Locate and identify every blood parasite.
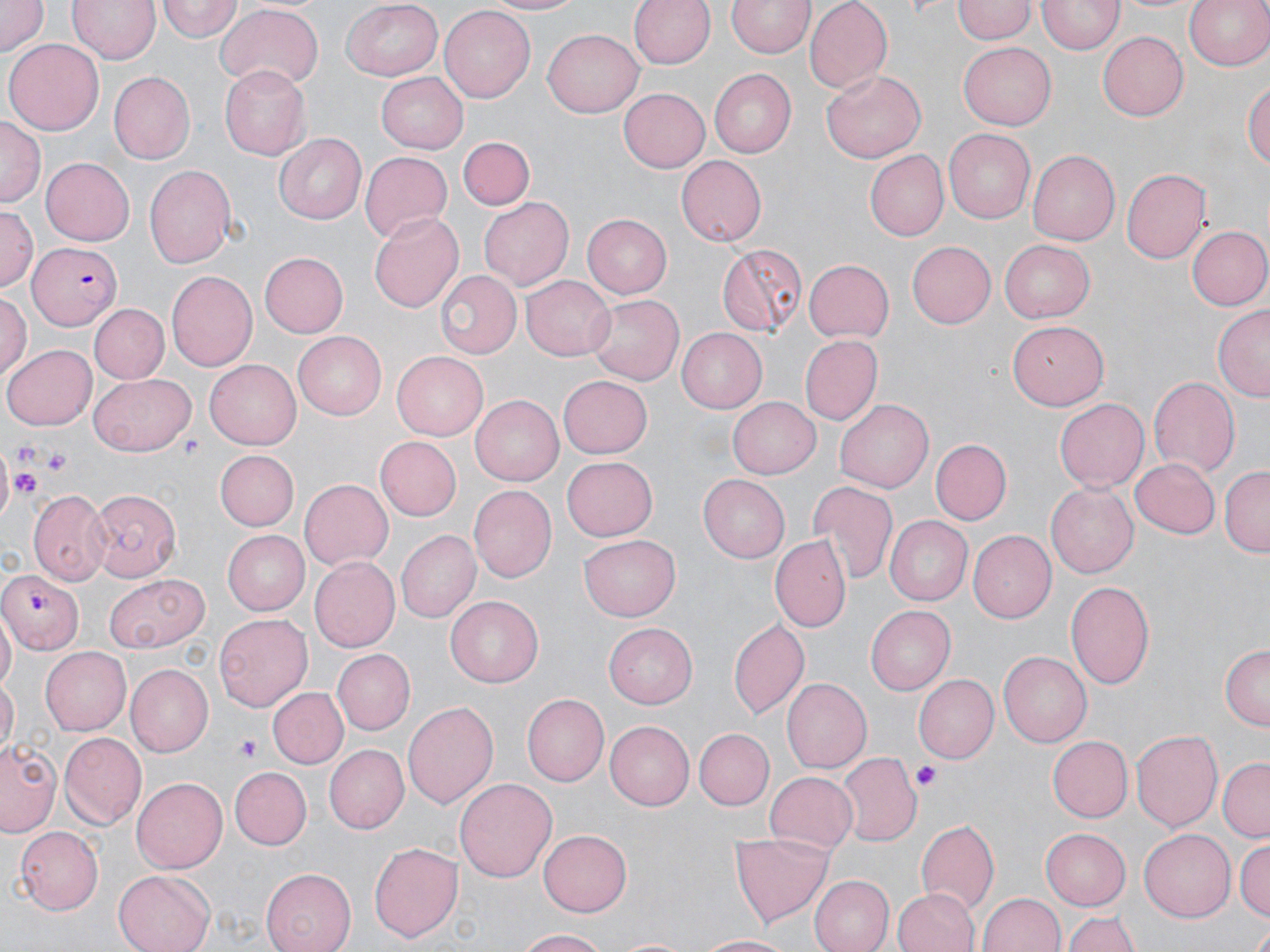
Approximate bounding boxes as (x1, y1, x2, y2) in pixels.
Plasmodium falciparum-infected red blood cells: (30, 240, 120, 331), (0, 569, 84, 653).
No Plasmodium ovale, Plasmodium malariae, Plasmodium vivax, Babesia divergens, or Trypanosoma brucei observed.

Platelet locations: (13, 444, 38, 470), (46, 450, 71, 476), (8, 468, 43, 500), (236, 735, 265, 759), (910, 762, 942, 791). Uninfected red blood cell locations: (0, 0, 48, 57), (68, 0, 160, 65), (478, 0, 589, 17), (630, 0, 715, 70), (804, 0, 892, 91), (1115, 0, 1211, 17), (1184, 0, 1270, 72), (158, 1, 241, 44), (340, 1, 444, 80), (727, 1, 813, 59), (953, 2, 1036, 44), (1038, 2, 1121, 55), (214, 5, 326, 88), (439, 6, 533, 104), (543, 28, 643, 116), (1098, 30, 1187, 119), (5, 39, 104, 136), (960, 41, 1055, 129), (218, 64, 310, 159), (709, 69, 796, 158), (822, 69, 926, 164), (108, 71, 195, 165), (375, 72, 468, 152), (1245, 76, 1270, 177), (618, 86, 712, 172), (0, 119, 44, 205), (943, 129, 1035, 224), (273, 133, 366, 224), (458, 134, 535, 210), (1028, 150, 1119, 244), (360, 151, 452, 242), (866, 152, 948, 240), (675, 155, 766, 247), (40, 156, 135, 246), (144, 166, 239, 270), (1121, 168, 1210, 266), (477, 195, 574, 292), (0, 206, 37, 298), (369, 211, 464, 314), (582, 214, 673, 298), (1186, 225, 1270, 311), (996, 239, 1094, 323), (906, 241, 995, 329), (715, 242, 807, 339), (261, 252, 349, 337), (803, 257, 894, 340), (436, 270, 520, 360), (168, 272, 257, 371), (520, 274, 615, 362), (0, 292, 30, 379), (586, 294, 685, 386), (90, 304, 169, 383), (1214, 306, 1269, 402), (1005, 321, 1102, 409), (677, 327, 768, 411), (294, 332, 387, 420), (800, 336, 882, 424), (3, 343, 95, 430), (391, 352, 487, 440), (206, 358, 306, 449), (90, 374, 195, 457), (558, 374, 652, 460), (1150, 376, 1239, 477), (469, 395, 562, 485), (1056, 395, 1149, 488), (727, 396, 819, 479), (836, 398, 933, 493), (376, 437, 462, 520), (933, 439, 1010, 524), (215, 450, 298, 530), (562, 455, 657, 541), (1130, 455, 1222, 537), (1220, 466, 1269, 554), (698, 473, 789, 562), (300, 479, 392, 571), (806, 479, 899, 586), (1046, 482, 1137, 579), (90, 485, 180, 584), (469, 485, 556, 583), (29, 490, 110, 585), (884, 517, 971, 606), (968, 529, 1057, 621), (224, 531, 308, 616), (395, 531, 480, 623), (773, 534, 852, 630), (580, 536, 679, 621), (310, 555, 399, 652), (102, 571, 210, 652), (1063, 582, 1155, 690), (446, 596, 543, 688), (866, 603, 955, 692), (214, 613, 311, 713), (1, 614, 16, 692), (728, 620, 809, 718), (604, 623, 698, 709), (1219, 644, 1269, 730), (40, 646, 131, 735), (331, 648, 415, 735), (996, 650, 1092, 746), (124, 665, 213, 757), (914, 675, 998, 764), (1, 677, 17, 752), (782, 678, 870, 773), (267, 684, 349, 768), (520, 692, 608, 787), (403, 702, 498, 810), (606, 720, 694, 810), (695, 729, 773, 809), (1132, 730, 1222, 832), (57, 733, 145, 827), (1046, 736, 1131, 822), (1, 738, 62, 837), (326, 745, 409, 833), (838, 753, 919, 846), (1220, 758, 1270, 841), (230, 767, 310, 848), (764, 772, 859, 851), (132, 777, 228, 873), (454, 777, 557, 883), (915, 819, 999, 916), (13, 825, 104, 912), (1040, 828, 1131, 910), (1138, 828, 1235, 921), (539, 831, 631, 915), (732, 833, 832, 924), (1235, 838, 1268, 920), (368, 842, 464, 943), (261, 868, 356, 952), (114, 870, 215, 952), (810, 873, 893, 952), (893, 887, 978, 952), (978, 892, 1066, 952), (1062, 909, 1141, 952), (1247, 926, 1270, 952), (515, 929, 613, 952), (696, 933, 794, 951), (612, 935, 691, 952). Slide-level diagnosis: Plasmodium falciparum. Single field of view. Optical microscopy. Thin blood film. Captured at 1000x magnification. Image is 1270×952 pixels. May-Grünwald-Giemsa stain.